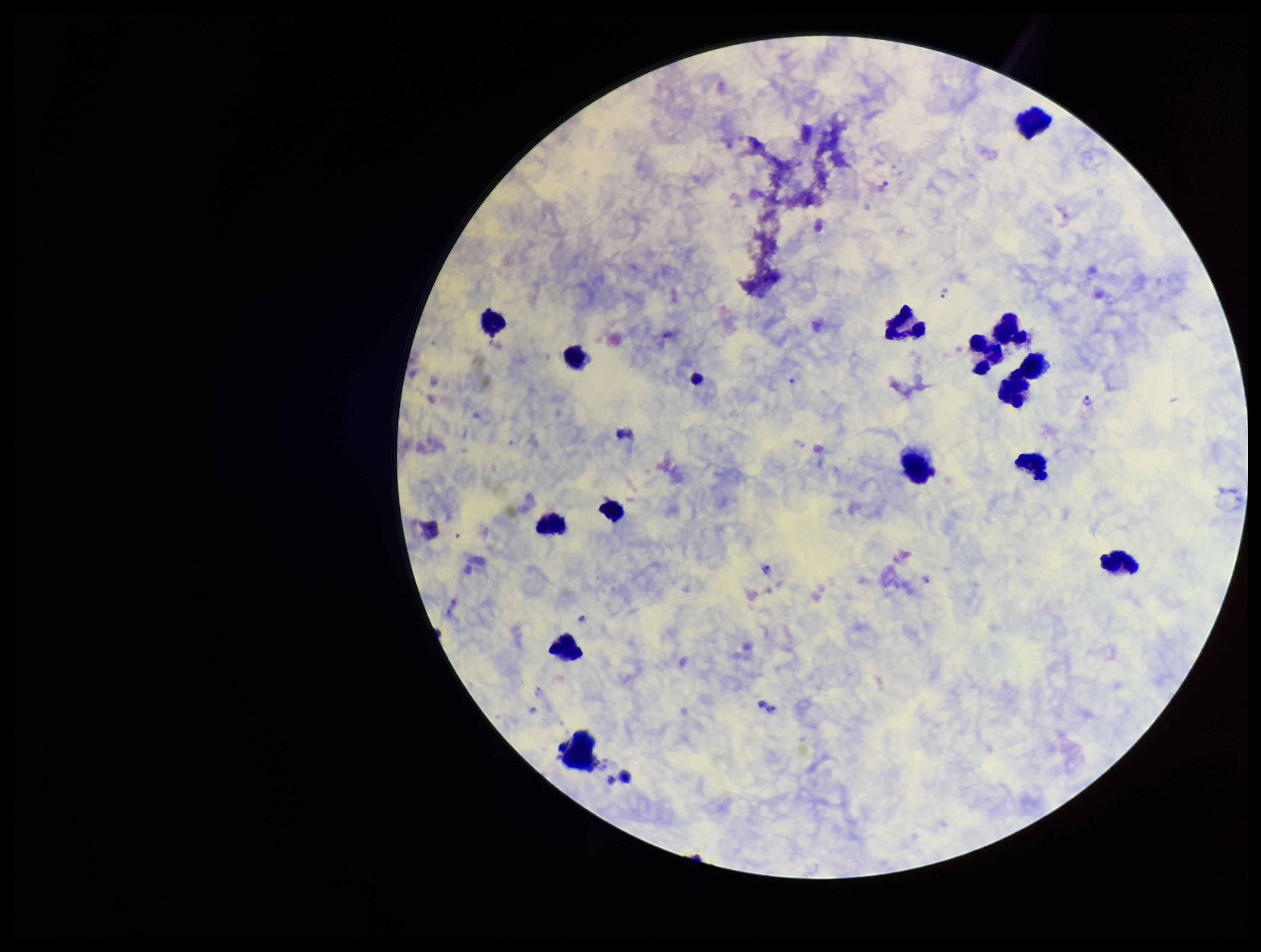 Leukocyte count: 15. One field from this slide. Preparation: thick smear. Image is 1261×952 pixels. Parasite count: 5. Stained with Giemsa. Patient malaria status: infected. Photographed through the microscope eyepiece with a smartphone camera. Species reported for this patient: Plasmodium vivax. Plasmodium parasites: identified.